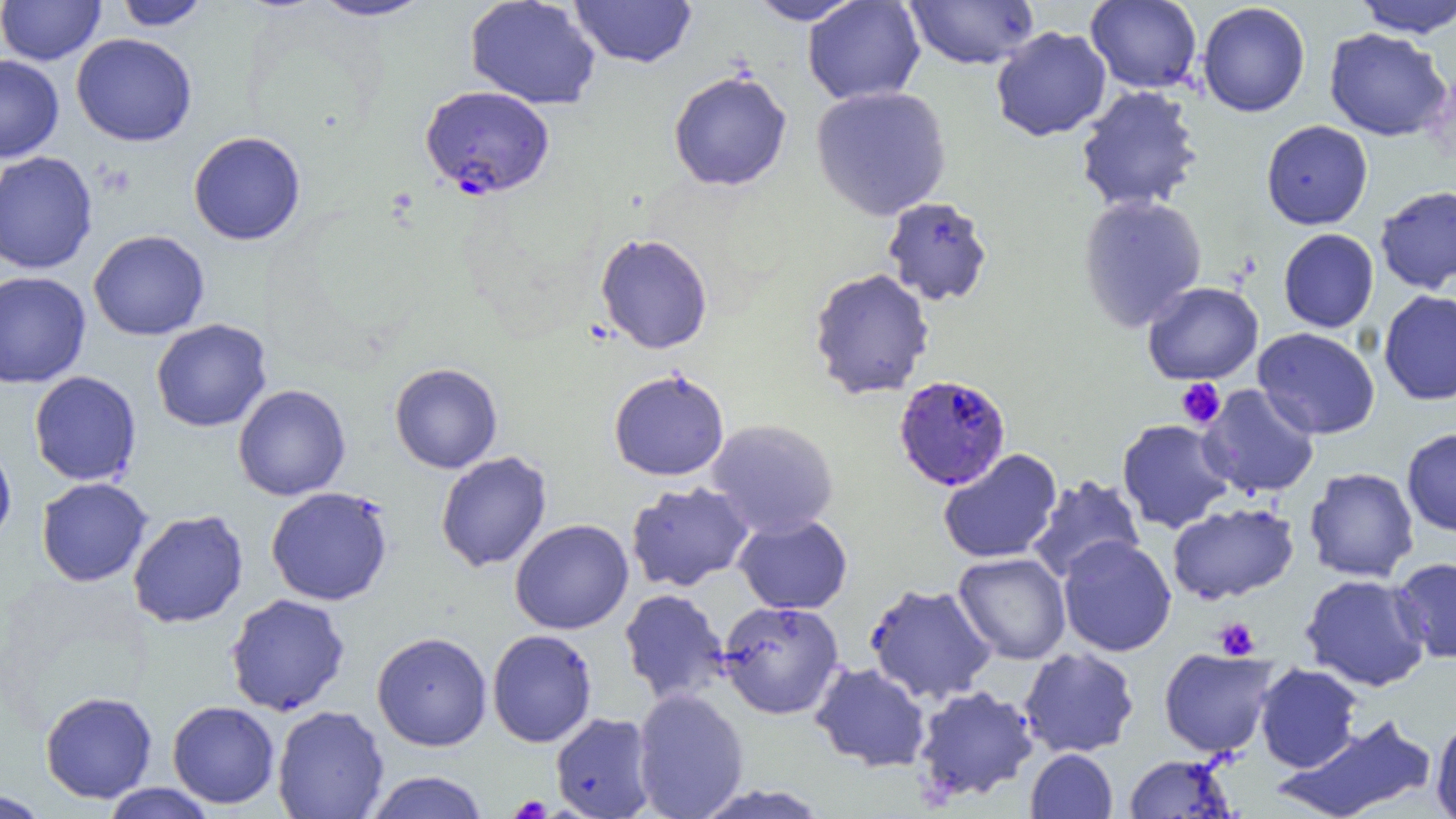

slide_level_diagnosis: Plasmodium falciparum
image_size: 1456×819 pixels
preparation: thin blood film
platelet_locations: 'approximate bounding boxes as [x1, y1, x2, y2] in pixels: [1176, 378, 1225, 428], [1214, 617, 1260, 660], [508, 795, 551, 818]'
field_of_view: single
uninfected_red_blood_cell_locations_subset: 'approximate bounding boxes as [x1, y1, x2, y2] in pixels: [1, 0, 105, 65], [114, 0, 212, 31], [309, 0, 434, 22], [464, 0, 601, 110], [569, 0, 697, 68], [746, 0, 866, 25], [802, 0, 926, 105], [904, 0, 1040, 70], [1085, 0, 1203, 94], [1353, 0, 1456, 37], [1197, 2, 1310, 117], [990, 26, 1112, 142], [1323, 28, 1451, 141], [71, 33, 197, 147], [0, 54, 64, 163], [667, 70, 792, 192], [810, 85, 952, 221], [1075, 86, 1204, 214], [1261, 120, 1373, 230], [188, 131, 306, 246], [0, 151, 98, 274], [1375, 186, 1456, 293], [1077, 193, 1208, 332], [882, 197, 994, 307], [1278, 228, 1379, 332], [88, 230, 210, 340], [595, 233, 713, 355], [808, 268, 935, 400], [0, 271, 92, 388], [1142, 281, 1263, 385], [1378, 290, 1456, 405], [151, 319, 272, 432], [1253, 327, 1380, 440], [389, 362, 503, 474], [608, 369, 730, 481], [29, 371, 142, 486], [232, 384, 351, 501], [1198, 384, 1321, 499], [1116, 418, 1235, 533], [705, 419, 839, 538], [1402, 428, 1456, 537], [0, 441, 17, 546], [938, 449, 1062, 564], [435, 451, 552, 573], [1304, 467, 1419, 583], [1025, 475, 1146, 584], [36, 477, 153, 587], [625, 482, 755, 592], [1167, 502, 1299, 604], [127, 509, 249, 628], [733, 514, 853, 614], [509, 519, 634, 635], [1057, 536, 1177, 656], [953, 552, 1071, 664], [1393, 557, 1456, 664], [1300, 573, 1431, 692], [864, 582, 998, 704], [619, 588, 731, 706], [225, 593, 350, 716], [717, 600, 845, 720], [487, 629, 598, 747], [371, 631, 493, 751], [1018, 647, 1140, 758], [1159, 648, 1280, 758], [809, 662, 932, 772], [1253, 663, 1363, 773], [913, 685, 1040, 803], [632, 687, 749, 819], [40, 690, 158, 803], [166, 700, 280, 809], [272, 705, 389, 819], [550, 712, 657, 819], [1277, 713, 1438, 819], [1430, 715, 1456, 818], [1025, 749, 1117, 819], [1124, 754, 1237, 818], [363, 771, 490, 819], [100, 782, 220, 818], [690, 783, 834, 819], [1, 789, 52, 818]'
modality: light microscopy
magnification: 1000x
plasmodium_falciparum_infected_red_blood_cell_locations_subset: 'approximate bounding boxes as [x1, y1, x2, y2] in pixels: [419, 85, 555, 199], [894, 374, 1011, 491]'